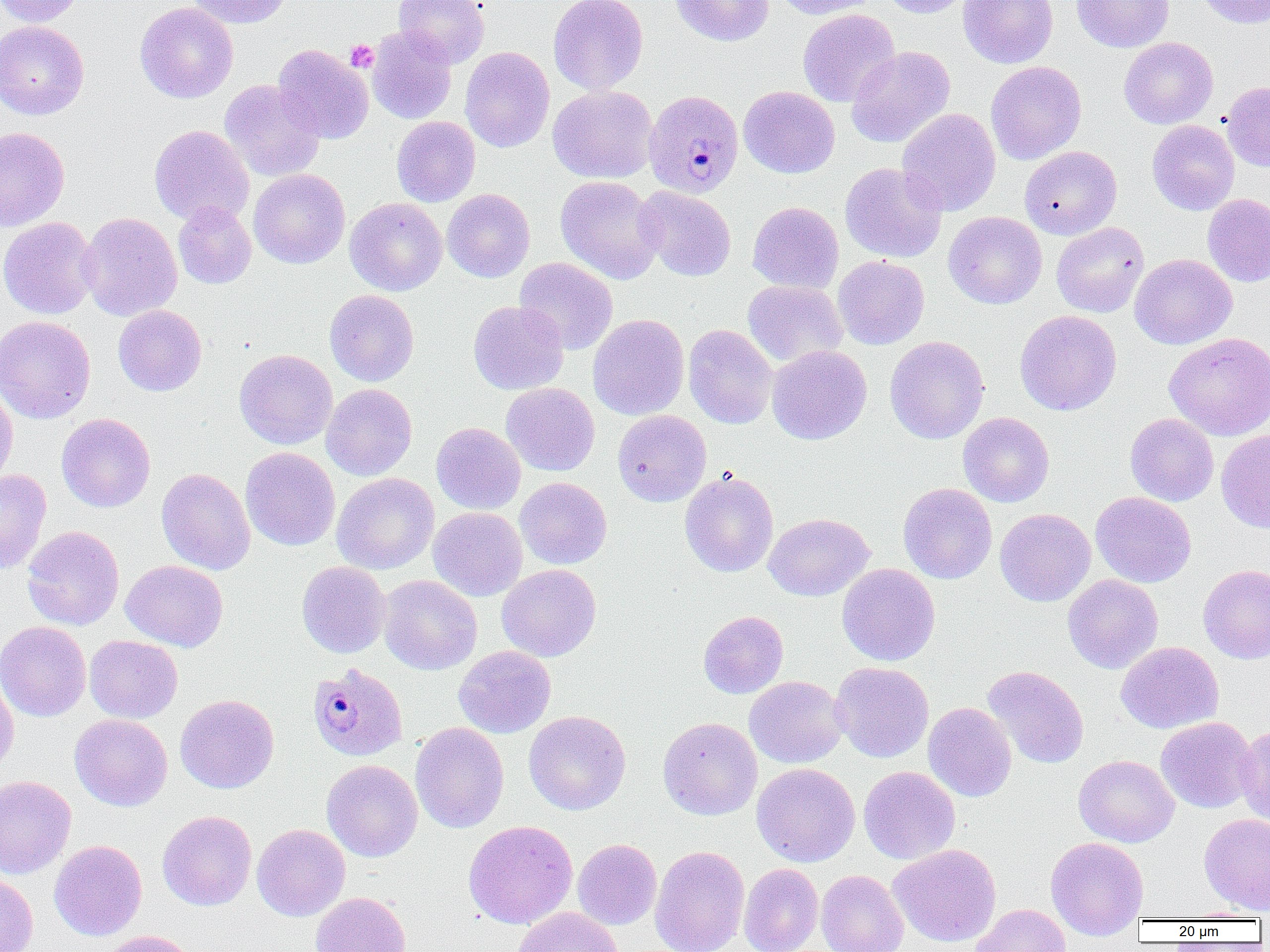 Approximate bounding boxes as named x1/y1/x2/y2 corners in pixels. Platelet locations: (x1=345, y1=40, x2=378, y2=72). Plasmodium malariae-infected red blood cell locations: (x1=646, y1=89, x2=747, y2=199), (x1=303, y1=666, x2=404, y2=764). Uninfected red blood cell locations: (x1=0, y1=0, x2=86, y2=26), (x1=186, y1=0, x2=292, y2=28), (x1=393, y1=0, x2=490, y2=67), (x1=548, y1=0, x2=648, y2=95), (x1=670, y1=0, x2=774, y2=46), (x1=775, y1=0, x2=880, y2=20), (x1=879, y1=0, x2=974, y2=18), (x1=959, y1=0, x2=1058, y2=68), (x1=1072, y1=0, x2=1174, y2=53), (x1=1195, y1=0, x2=1270, y2=28), (x1=135, y1=2, x2=238, y2=103), (x1=797, y1=9, x2=900, y2=107), (x1=0, y1=20, x2=89, y2=120), (x1=367, y1=26, x2=457, y2=124), (x1=1119, y1=37, x2=1218, y2=129), (x1=272, y1=45, x2=373, y2=143), (x1=846, y1=45, x2=955, y2=148), (x1=460, y1=47, x2=554, y2=152), (x1=986, y1=61, x2=1086, y2=164), (x1=219, y1=80, x2=325, y2=182), (x1=1221, y1=81, x2=1270, y2=172), (x1=548, y1=85, x2=658, y2=184), (x1=738, y1=86, x2=840, y2=178), (x1=897, y1=108, x2=1001, y2=216), (x1=392, y1=116, x2=480, y2=207), (x1=1147, y1=120, x2=1239, y2=215), (x1=149, y1=125, x2=254, y2=227), (x1=0, y1=127, x2=69, y2=231), (x1=1020, y1=146, x2=1121, y2=239), (x1=839, y1=162, x2=948, y2=263), (x1=248, y1=169, x2=350, y2=269), (x1=555, y1=176, x2=664, y2=284), (x1=635, y1=186, x2=736, y2=281), (x1=442, y1=189, x2=535, y2=282), (x1=1202, y1=194, x2=1270, y2=287), (x1=345, y1=197, x2=447, y2=296), (x1=173, y1=201, x2=256, y2=289), (x1=748, y1=201, x2=844, y2=294), (x1=943, y1=211, x2=1047, y2=309), (x1=78, y1=212, x2=182, y2=321), (x1=0, y1=217, x2=99, y2=319), (x1=1051, y1=222, x2=1149, y2=317), (x1=1130, y1=254, x2=1237, y2=349), (x1=833, y1=255, x2=929, y2=349), (x1=514, y1=257, x2=618, y2=355), (x1=742, y1=279, x2=847, y2=367), (x1=324, y1=289, x2=419, y2=386), (x1=468, y1=300, x2=569, y2=395), (x1=113, y1=304, x2=207, y2=396), (x1=1014, y1=310, x2=1121, y2=415), (x1=588, y1=314, x2=689, y2=421), (x1=0, y1=315, x2=95, y2=424), (x1=683, y1=324, x2=777, y2=429), (x1=1164, y1=332, x2=1270, y2=440), (x1=885, y1=335, x2=989, y2=444), (x1=767, y1=345, x2=871, y2=445), (x1=234, y1=349, x2=337, y2=449), (x1=0, y1=382, x2=18, y2=489), (x1=501, y1=383, x2=599, y2=476), (x1=321, y1=384, x2=417, y2=480), (x1=613, y1=410, x2=711, y2=506), (x1=958, y1=412, x2=1054, y2=507), (x1=56, y1=413, x2=156, y2=512), (x1=1125, y1=413, x2=1218, y2=506), (x1=431, y1=422, x2=526, y2=514), (x1=1216, y1=429, x2=1270, y2=533), (x1=240, y1=447, x2=340, y2=551), (x1=156, y1=468, x2=255, y2=575), (x1=0, y1=469, x2=51, y2=575), (x1=680, y1=470, x2=778, y2=577), (x1=331, y1=472, x2=439, y2=574), (x1=514, y1=477, x2=612, y2=569), (x1=898, y1=483, x2=997, y2=584), (x1=1091, y1=492, x2=1196, y2=588), (x1=428, y1=507, x2=527, y2=601), (x1=995, y1=508, x2=1096, y2=606), (x1=763, y1=513, x2=875, y2=601), (x1=22, y1=525, x2=124, y2=630), (x1=120, y1=560, x2=228, y2=651), (x1=296, y1=561, x2=391, y2=658), (x1=497, y1=563, x2=601, y2=662), (x1=837, y1=563, x2=940, y2=666), (x1=1198, y1=564, x2=1270, y2=664), (x1=1062, y1=574, x2=1163, y2=674), (x1=378, y1=575, x2=482, y2=675), (x1=698, y1=610, x2=789, y2=699), (x1=0, y1=620, x2=91, y2=722), (x1=84, y1=635, x2=183, y2=723), (x1=1116, y1=641, x2=1224, y2=734), (x1=453, y1=646, x2=556, y2=738), (x1=830, y1=662, x2=934, y2=763), (x1=982, y1=666, x2=1089, y2=769), (x1=0, y1=667, x2=19, y2=777), (x1=744, y1=676, x2=848, y2=768), (x1=175, y1=694, x2=279, y2=794), (x1=923, y1=702, x2=1017, y2=802), (x1=523, y1=710, x2=631, y2=815), (x1=69, y1=714, x2=172, y2=810), (x1=658, y1=717, x2=762, y2=820), (x1=1155, y1=717, x2=1259, y2=813), (x1=410, y1=722, x2=509, y2=833), (x1=1236, y1=724, x2=1270, y2=826), (x1=1074, y1=755, x2=1179, y2=847), (x1=322, y1=760, x2=422, y2=862), (x1=752, y1=763, x2=860, y2=867), (x1=858, y1=766, x2=960, y2=864), (x1=0, y1=775, x2=76, y2=879), (x1=157, y1=810, x2=257, y2=911), (x1=1199, y1=813, x2=1270, y2=915), (x1=462, y1=819, x2=578, y2=929), (x1=252, y1=824, x2=350, y2=921), (x1=1046, y1=836, x2=1149, y2=939), (x1=573, y1=839, x2=661, y2=930), (x1=49, y1=840, x2=147, y2=941), (x1=889, y1=844, x2=1001, y2=947), (x1=649, y1=845, x2=749, y2=952), (x1=739, y1=863, x2=823, y2=952), (x1=816, y1=870, x2=909, y2=952), (x1=0, y1=872, x2=38, y2=952), (x1=489, y1=874, x2=599, y2=950), (x1=309, y1=891, x2=411, y2=952), (x1=971, y1=904, x2=1071, y2=952), (x1=511, y1=906, x2=624, y2=952), (x1=1182, y1=908, x2=1266, y2=921), (x1=91, y1=930, x2=197, y2=952). Slide-level diagnosis: Plasmodium malariae. Thin blood smear. Image is 1270×952 pixels. 1000x magnification. One field of a larger specimen. Optical microscopy.